Assess the morphology of the red blood cells.
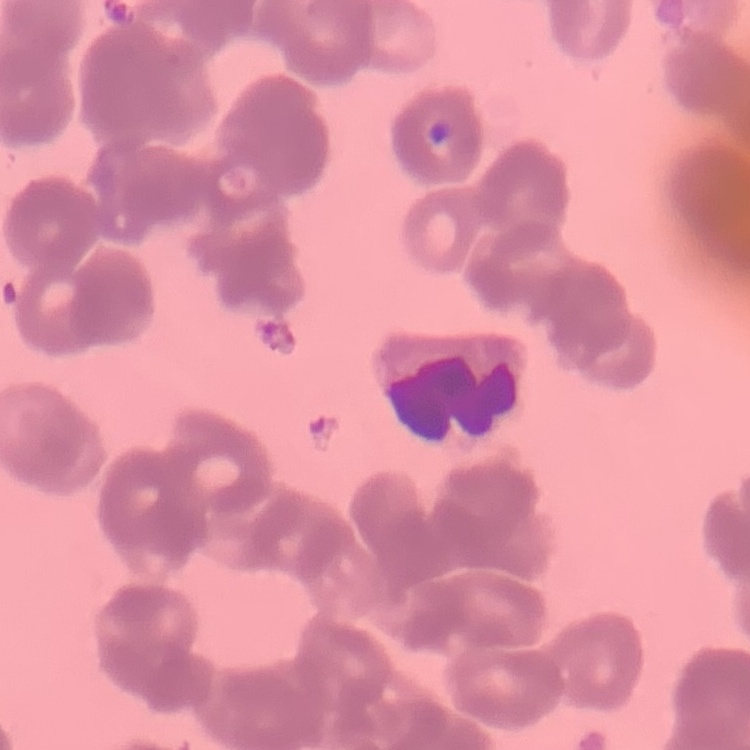
They show rouleaux formation.

{
  "preparation": "thin blood smear",
  "stain": "Field's or Giemsa",
  "image_type": "square crop of a larger photomicrograph"
}